Classify this cell by malaria status.
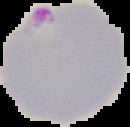

Parasitized.

image size = 130×127 pixels
image type = segmented cell region with the area outside set to black
preparation = thin blood film